Assess this cell for malaria.
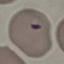

It is parasitized.

Summary:
  - Stain: Giemsa
  - Image type: cell patch, automatically extracted from a larger field of view and resized to 64 × 64 pixels
  - Capture: smartphone through the microscope eyepiece
  - Preparation: thin blood film